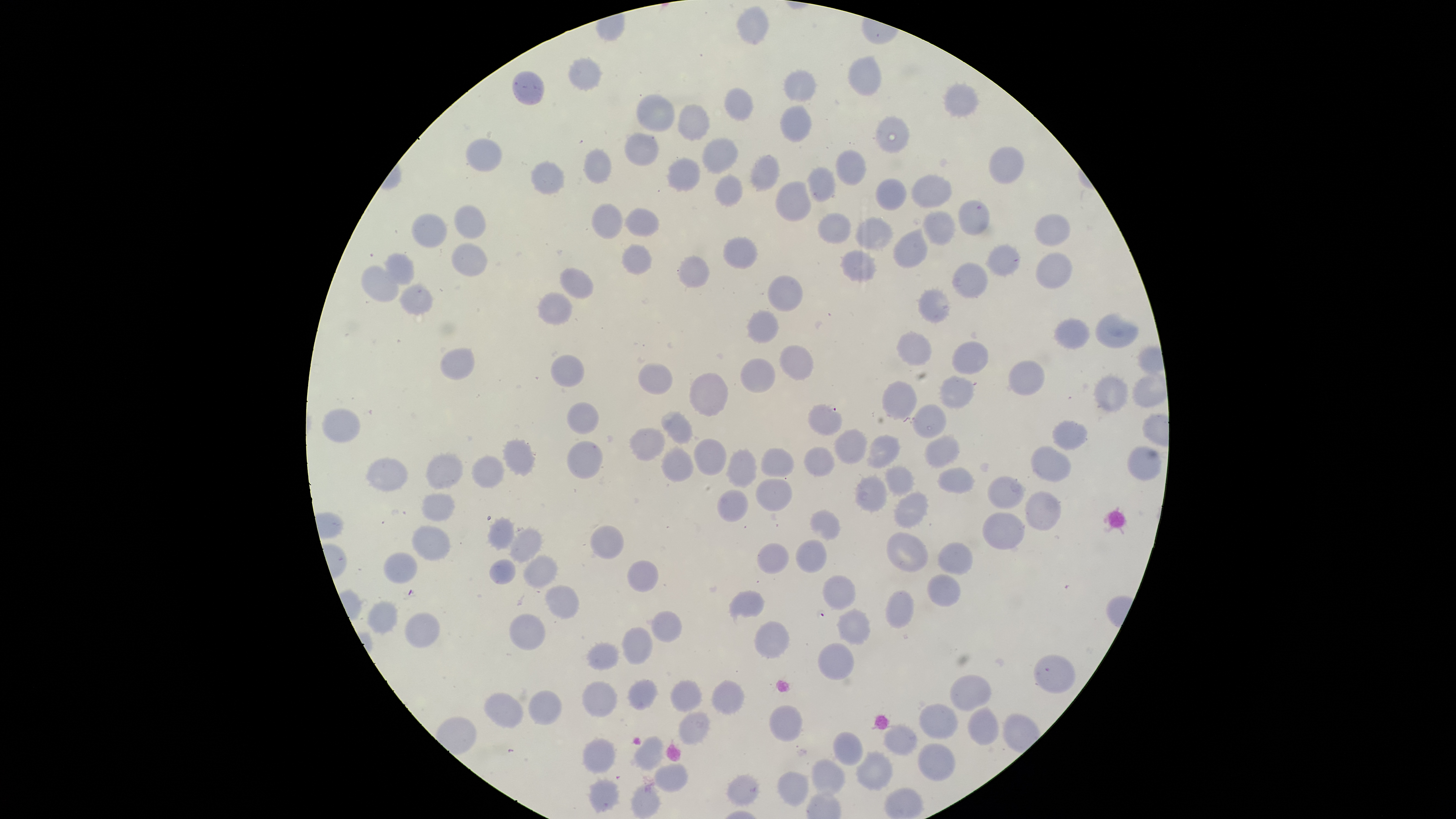

image size = 1456×819 pixels
presence = no malaria parasites detected
preparation = thin smear of blood
stain = Giemsa
visible region = circular
uninfected RBCs = approximate bounding boxes as [left, top, right, bottom] in pixels: [739, 6, 769, 43], [849, 57, 883, 97], [568, 59, 602, 90], [785, 69, 818, 101], [512, 71, 544, 105], [945, 84, 980, 116], [725, 89, 752, 121], [637, 94, 674, 131], [678, 105, 709, 141], [781, 106, 812, 141], [877, 115, 910, 152], [625, 132, 659, 166], [466, 138, 501, 171], [703, 138, 737, 173], [988, 146, 1024, 184], [584, 148, 611, 183], [837, 151, 866, 184], [752, 155, 778, 191], [668, 158, 698, 191], [531, 160, 564, 195], [808, 167, 836, 201], [716, 174, 742, 206], [912, 175, 952, 207], [877, 179, 906, 211], [775, 181, 810, 221], [959, 202, 989, 236], [455, 203, 486, 239], [592, 203, 622, 239], [627, 208, 659, 236], [922, 211, 955, 245], [412, 212, 447, 248], [819, 212, 850, 244], [1034, 215, 1069, 246], [856, 217, 894, 250], [894, 227, 928, 268], [723, 238, 758, 269], [452, 242, 487, 277], [622, 243, 652, 274], [987, 243, 1020, 276], [841, 250, 877, 282], [385, 253, 414, 284], [1037, 253, 1073, 290], [679, 256, 709, 288], [954, 261, 988, 299], [360, 264, 399, 302], [560, 268, 593, 299], [769, 275, 803, 311], [400, 284, 432, 315], [918, 290, 951, 323], [538, 292, 571, 325], [748, 310, 779, 344], [1096, 312, 1139, 346], [1055, 319, 1090, 348], [897, 331, 932, 367], [953, 341, 989, 375], [780, 345, 812, 381], [441, 348, 474, 380], [551, 353, 584, 387], [740, 359, 775, 393], [1008, 359, 1046, 395], [638, 362, 672, 394], [690, 373, 728, 416], [1095, 374, 1129, 412], [1134, 375, 1167, 406], [941, 376, 974, 408], [881, 380, 917, 419], [568, 401, 599, 433], [913, 403, 946, 438], [809, 404, 842, 435], [323, 409, 360, 443], [662, 411, 692, 443], [1053, 420, 1087, 449], [629, 428, 665, 461], [835, 428, 867, 465], [869, 435, 901, 467], [926, 435, 960, 469], [694, 437, 726, 476], [503, 439, 534, 476], [568, 441, 603, 479], [805, 446, 834, 475], [1127, 446, 1162, 480], [1031, 447, 1072, 481], [663, 448, 693, 481], [728, 448, 756, 487], [762, 448, 793, 476], [426, 454, 463, 490], [471, 455, 504, 490], [367, 457, 407, 492], [884, 466, 915, 495], [938, 467, 975, 493], [855, 475, 888, 511], [988, 475, 1023, 507], [757, 479, 793, 511], [718, 488, 749, 522], [894, 490, 929, 528], [1025, 490, 1061, 530], [422, 493, 455, 521], [810, 511, 841, 539], [983, 511, 1024, 551], [489, 516, 514, 551], [411, 525, 452, 560], [590, 525, 624, 559], [512, 529, 541, 563], [887, 531, 928, 572], [795, 539, 827, 574], [939, 541, 973, 575], [757, 543, 790, 573], [383, 552, 418, 584], [526, 555, 557, 587], [489, 559, 515, 584], [627, 559, 658, 592], [928, 574, 961, 606], [823, 575, 857, 609], [546, 585, 579, 618], [729, 589, 765, 619], [887, 589, 915, 628], [368, 600, 398, 633], [838, 608, 870, 645], [651, 611, 682, 642], [405, 613, 440, 648], [510, 614, 545, 651], [754, 622, 790, 659], [622, 628, 652, 665], [587, 642, 619, 670], [819, 644, 854, 680], [1033, 655, 1076, 693], [950, 675, 991, 710], [628, 678, 657, 709], [671, 679, 702, 712], [713, 680, 745, 714], [583, 682, 616, 717], [528, 690, 561, 725], [485, 692, 524, 729], [921, 704, 959, 739], [969, 704, 1000, 745], [770, 706, 801, 742], [679, 711, 710, 745], [883, 724, 917, 757], [832, 732, 863, 764], [633, 737, 663, 769], [582, 738, 614, 773], [917, 742, 956, 781], [858, 751, 894, 790], [812, 761, 844, 794], [656, 764, 687, 792], [778, 771, 808, 806], [727, 775, 759, 806], [588, 779, 620, 811], [631, 785, 659, 817]
capture = smartphone photograph through the microscope eyepiece
field of view = single